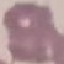
{
  "malaria_status": "uninfected",
  "capture": "smartphone camera at the microscope eyepiece",
  "image_type": "automatically extracted cell patch, resized to 64 × 64 pixels",
  "preparation": "thin blood film",
  "stain": "Giemsa"
}